Name the parasite shown.
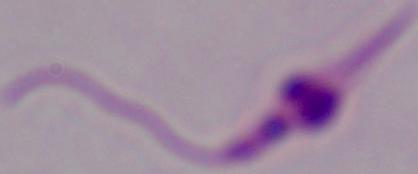
This is Leishmania.

Captured at 1000x magnification. Photomicrograph.